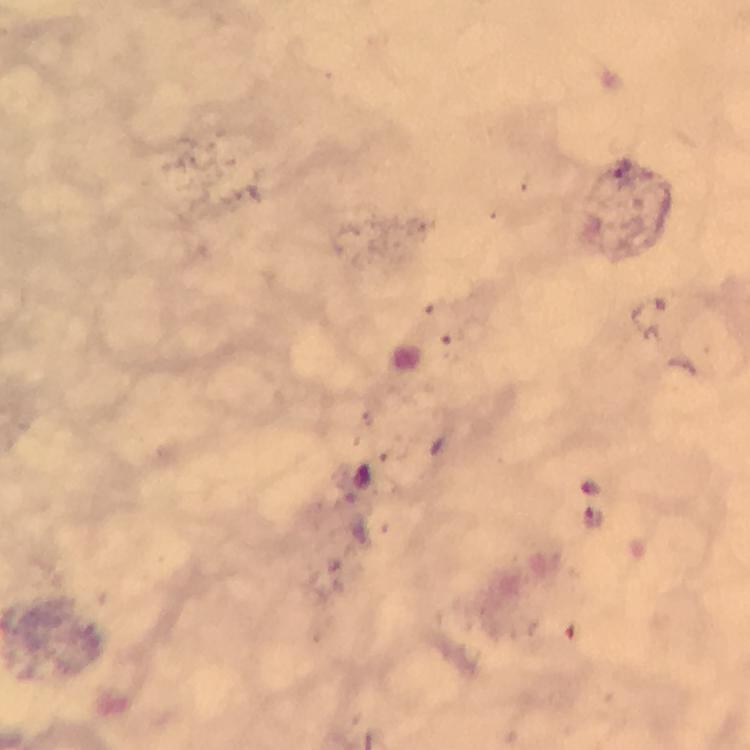
preparation: thick blood smear
malaria_parasite_locations: 'approximate object centers, in pixels from the top-left corner: (x=623, y=167), (x=591, y=517)'
immersion_oil: used
cropped_from: a single field of view
magnification: 100x
capture: smartphone photograph through a microscope
context: from a malaria diagnostic workup
stain: Giemsa
image_size: 750×750 pixels